Locate and identify every blood parasite.
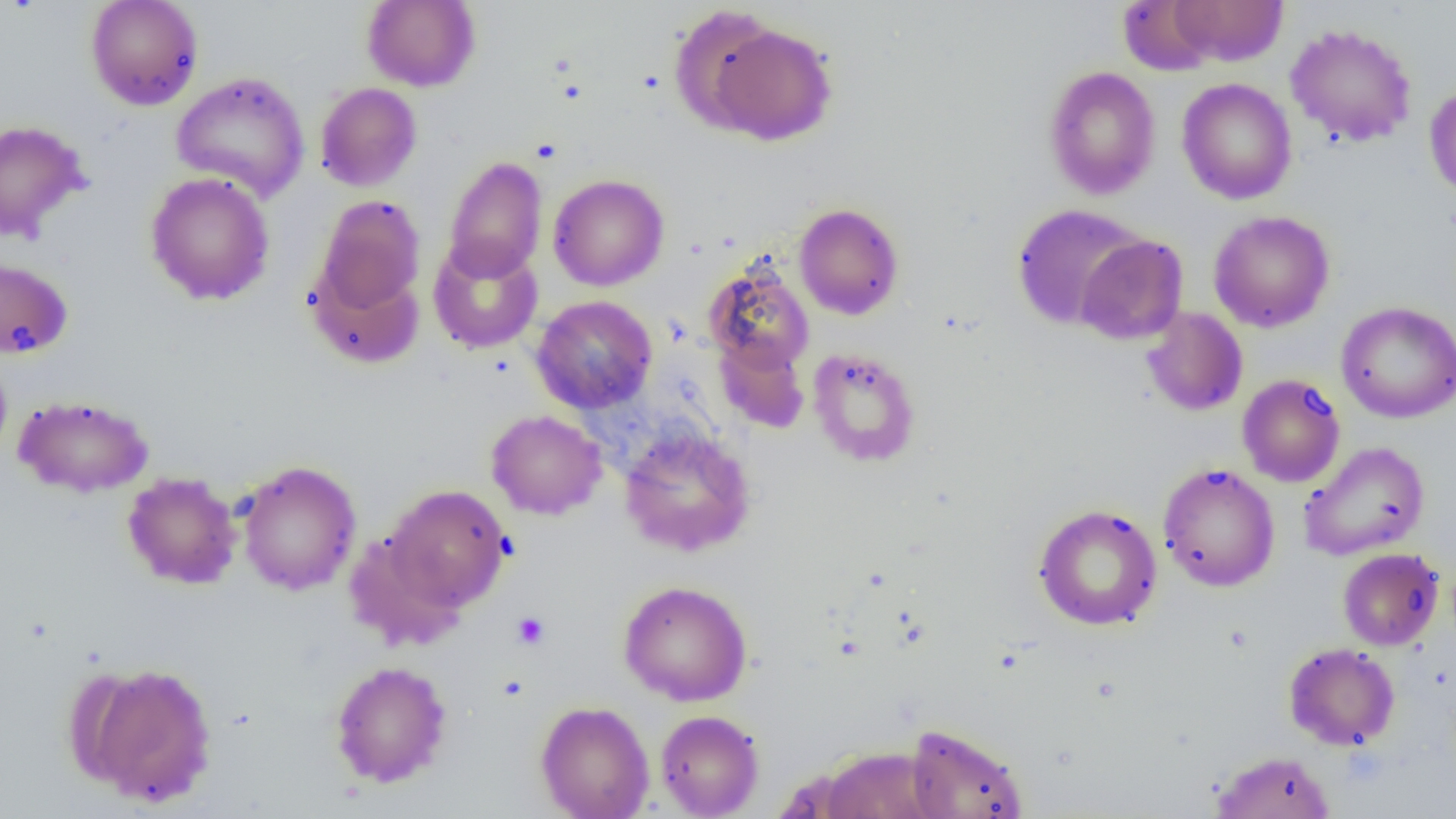

No blood parasites seen.

slide-level diagnosis = no evidence of blood parasites
preparation = thin blood film
image size = 1456×819 pixels
uninfected red blood cell locations = approximate bounding boxes as [x1, y1, x2, y2] in pixels: [85, 0, 203, 110], [1117, 0, 1220, 76], [1168, 0, 1288, 66], [362, 1, 480, 91], [669, 4, 783, 134], [707, 21, 838, 145], [1285, 23, 1418, 148], [1043, 65, 1161, 200], [171, 71, 311, 202], [1176, 78, 1297, 205], [314, 82, 422, 192], [1424, 83, 1456, 202], [0, 119, 90, 243], [443, 156, 547, 282], [145, 172, 275, 306], [548, 174, 669, 291], [313, 196, 425, 319], [793, 202, 904, 320], [1010, 204, 1147, 331], [1208, 211, 1335, 333], [1076, 234, 1188, 344], [428, 237, 543, 354], [0, 256, 74, 360], [307, 259, 425, 369], [703, 259, 815, 373], [531, 295, 657, 414], [1336, 301, 1456, 423], [1142, 307, 1248, 416], [714, 335, 810, 434], [807, 347, 921, 468], [0, 354, 12, 464], [1237, 374, 1345, 487], [13, 394, 154, 498], [486, 409, 607, 520], [619, 426, 756, 557], [1299, 440, 1430, 561], [237, 461, 362, 595], [1158, 463, 1280, 592], [122, 472, 241, 589], [382, 484, 512, 612], [1033, 503, 1163, 631], [1337, 547, 1444, 650], [618, 580, 752, 706], [1284, 642, 1400, 750], [329, 660, 452, 788], [78, 662, 217, 807], [535, 700, 654, 819], [655, 710, 764, 818], [904, 723, 1029, 819], [819, 746, 942, 819], [1211, 750, 1335, 819]
platelet locations = approximate bounding boxes as [x1, y1, x2, y2] in pixels: [511, 611, 550, 650]
magnification = 1000x
field of view = single
modality = optical microscopy